Assess the morphology of the erythrocytes.
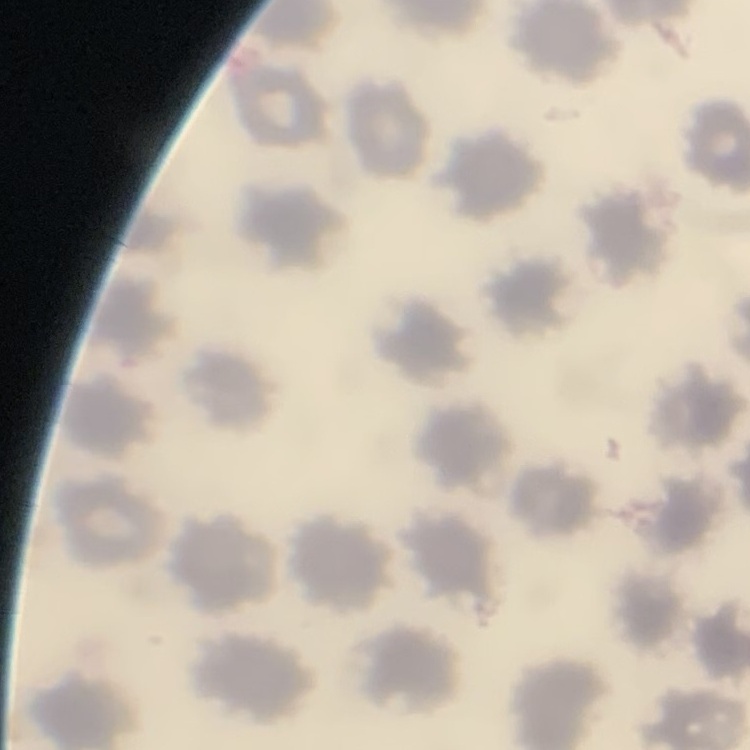
They show no rouleaux formation.

preparation = thin blood smear
image type = square crop of a larger photomicrograph
stain = Field's or Giemsa